Locate and identify every blood parasite.
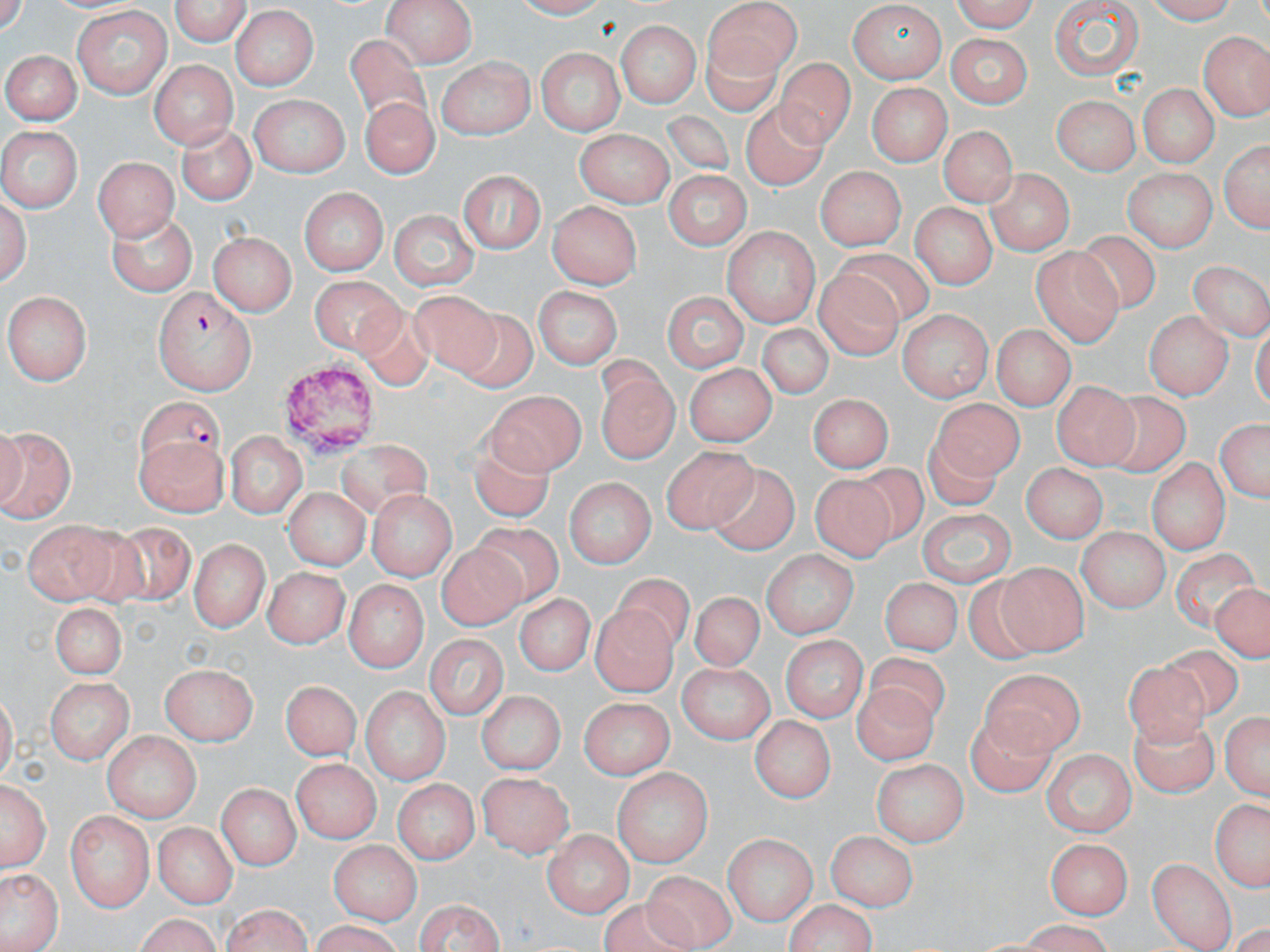
Approximate bounding boxes as named x1/y1/x2/y2 corners in pixels.
Plasmodium falciparum-infected red blood cells: (x1=152, y1=289, x2=257, y2=394), (x1=137, y1=400, x2=225, y2=473).
No Plasmodium ovale, Plasmodium malariae, Plasmodium vivax, Babesia divergens, or Trypanosoma brucei observed.

Summary:
  - Platelet locations: (x1=278, y1=363, x2=381, y2=454)
  - Uninfected red blood cell locations: (x1=169, y1=0, x2=252, y2=46), (x1=944, y1=0, x2=1039, y2=32), (x1=1147, y1=0, x2=1245, y2=27), (x1=384, y1=1, x2=475, y2=68), (x1=704, y1=1, x2=804, y2=88), (x1=1049, y1=3, x2=1144, y2=82), (x1=849, y1=4, x2=946, y2=79), (x1=72, y1=6, x2=172, y2=96), (x1=229, y1=9, x2=320, y2=89), (x1=949, y1=16, x2=1036, y2=72), (x1=613, y1=21, x2=703, y2=105), (x1=943, y1=32, x2=1032, y2=106), (x1=1202, y1=32, x2=1269, y2=120), (x1=701, y1=35, x2=777, y2=115), (x1=345, y1=38, x2=437, y2=145), (x1=536, y1=46, x2=624, y2=137), (x1=3, y1=49, x2=78, y2=126), (x1=775, y1=56, x2=850, y2=146), (x1=150, y1=57, x2=236, y2=146), (x1=434, y1=59, x2=532, y2=138), (x1=866, y1=83, x2=951, y2=165), (x1=1136, y1=84, x2=1222, y2=167), (x1=360, y1=95, x2=440, y2=176), (x1=1051, y1=96, x2=1137, y2=173), (x1=249, y1=97, x2=347, y2=175), (x1=734, y1=97, x2=837, y2=191), (x1=657, y1=107, x2=735, y2=177), (x1=176, y1=124, x2=255, y2=205), (x1=939, y1=125, x2=1013, y2=207), (x1=0, y1=126, x2=82, y2=211), (x1=572, y1=130, x2=671, y2=203), (x1=1218, y1=134, x2=1269, y2=237), (x1=94, y1=154, x2=174, y2=240), (x1=1122, y1=165, x2=1218, y2=252), (x1=456, y1=167, x2=546, y2=254), (x1=814, y1=167, x2=908, y2=247), (x1=661, y1=170, x2=752, y2=250), (x1=988, y1=171, x2=1072, y2=253), (x1=299, y1=187, x2=387, y2=278), (x1=2, y1=189, x2=31, y2=295), (x1=914, y1=198, x2=999, y2=287), (x1=550, y1=200, x2=643, y2=285), (x1=388, y1=210, x2=479, y2=292), (x1=107, y1=213, x2=198, y2=292), (x1=723, y1=225, x2=818, y2=325), (x1=211, y1=229, x2=297, y2=313), (x1=1075, y1=229, x2=1158, y2=313), (x1=833, y1=245, x2=937, y2=329), (x1=1033, y1=248, x2=1122, y2=346), (x1=1189, y1=260, x2=1270, y2=341), (x1=813, y1=267, x2=903, y2=365), (x1=310, y1=276, x2=408, y2=364), (x1=531, y1=288, x2=623, y2=369), (x1=660, y1=289, x2=749, y2=372), (x1=411, y1=290, x2=502, y2=385), (x1=6, y1=292, x2=92, y2=382), (x1=461, y1=302, x2=541, y2=399), (x1=354, y1=303, x2=434, y2=395), (x1=898, y1=308, x2=992, y2=402), (x1=1145, y1=312, x2=1229, y2=397), (x1=758, y1=324, x2=834, y2=407), (x1=992, y1=327, x2=1074, y2=412), (x1=686, y1=360, x2=779, y2=445), (x1=592, y1=370, x2=679, y2=467), (x1=1055, y1=381, x2=1135, y2=469), (x1=486, y1=390, x2=586, y2=475), (x1=806, y1=392, x2=897, y2=471), (x1=1102, y1=393, x2=1189, y2=475), (x1=934, y1=397, x2=1024, y2=483), (x1=1213, y1=417, x2=1270, y2=507), (x1=471, y1=422, x2=555, y2=520), (x1=0, y1=424, x2=76, y2=523), (x1=925, y1=430, x2=1005, y2=507), (x1=225, y1=431, x2=305, y2=519), (x1=135, y1=441, x2=231, y2=513), (x1=339, y1=441, x2=442, y2=516), (x1=663, y1=444, x2=753, y2=536), (x1=1148, y1=457, x2=1231, y2=552), (x1=701, y1=461, x2=800, y2=552), (x1=856, y1=461, x2=933, y2=540), (x1=1020, y1=462, x2=1105, y2=542), (x1=813, y1=472, x2=900, y2=564), (x1=563, y1=479, x2=656, y2=565), (x1=282, y1=486, x2=369, y2=571), (x1=368, y1=490, x2=455, y2=580), (x1=913, y1=507, x2=1016, y2=584), (x1=21, y1=515, x2=121, y2=604), (x1=469, y1=519, x2=561, y2=603), (x1=109, y1=520, x2=194, y2=601), (x1=1078, y1=526, x2=1169, y2=612), (x1=191, y1=536, x2=266, y2=633), (x1=436, y1=543, x2=524, y2=628), (x1=1171, y1=548, x2=1259, y2=637), (x1=758, y1=553, x2=857, y2=639), (x1=997, y1=562, x2=1085, y2=656), (x1=261, y1=567, x2=348, y2=645), (x1=615, y1=575, x2=691, y2=654), (x1=879, y1=575, x2=960, y2=662), (x1=967, y1=575, x2=1053, y2=666), (x1=341, y1=579, x2=428, y2=676), (x1=1208, y1=582, x2=1270, y2=660), (x1=692, y1=586, x2=766, y2=670), (x1=518, y1=592, x2=592, y2=676), (x1=45, y1=602, x2=128, y2=677), (x1=588, y1=604, x2=679, y2=698), (x1=424, y1=633, x2=508, y2=722), (x1=781, y1=636, x2=866, y2=724), (x1=1160, y1=638, x2=1255, y2=720), (x1=866, y1=650, x2=951, y2=734), (x1=674, y1=660, x2=776, y2=742), (x1=1123, y1=660, x2=1213, y2=751), (x1=162, y1=665, x2=257, y2=745), (x1=980, y1=671, x2=1090, y2=763), (x1=43, y1=675, x2=132, y2=763), (x1=279, y1=679, x2=359, y2=764), (x1=854, y1=680, x2=931, y2=762), (x1=360, y1=683, x2=449, y2=788), (x1=477, y1=690, x2=566, y2=774), (x1=577, y1=696, x2=673, y2=776), (x1=1220, y1=704, x2=1270, y2=804), (x1=967, y1=705, x2=1061, y2=795), (x1=750, y1=713, x2=835, y2=804), (x1=1129, y1=713, x2=1221, y2=798), (x1=101, y1=731, x2=201, y2=816), (x1=1042, y1=748, x2=1135, y2=836), (x1=290, y1=758, x2=378, y2=841), (x1=874, y1=760, x2=968, y2=845), (x1=614, y1=765, x2=713, y2=865), (x1=478, y1=768, x2=574, y2=858), (x1=219, y1=770, x2=372, y2=849), (x1=2, y1=776, x2=47, y2=873), (x1=394, y1=777, x2=478, y2=867), (x1=217, y1=779, x2=299, y2=870), (x1=1206, y1=798, x2=1270, y2=891), (x1=67, y1=812, x2=154, y2=912), (x1=152, y1=822, x2=234, y2=906), (x1=539, y1=826, x2=629, y2=918), (x1=828, y1=830, x2=916, y2=911), (x1=723, y1=833, x2=815, y2=925), (x1=329, y1=837, x2=420, y2=923), (x1=1045, y1=839, x2=1131, y2=920), (x1=1144, y1=860, x2=1230, y2=946), (x1=635, y1=869, x2=743, y2=947), (x1=4, y1=871, x2=59, y2=948), (x1=604, y1=895, x2=705, y2=952), (x1=412, y1=896, x2=507, y2=952), (x1=779, y1=898, x2=882, y2=952), (x1=220, y1=905, x2=315, y2=952), (x1=133, y1=914, x2=225, y2=952), (x1=302, y1=922, x2=411, y2=952)
  - Slide-level diagnosis: Plasmodium falciparum
  - Magnification: 1000x
  - Modality: light microscopy
  - Stain: May-Grünwald-Giemsa
  - Field of view: one of a larger specimen
  - Image size: 1270×952 pixels
  - Preparation: thin blood smear